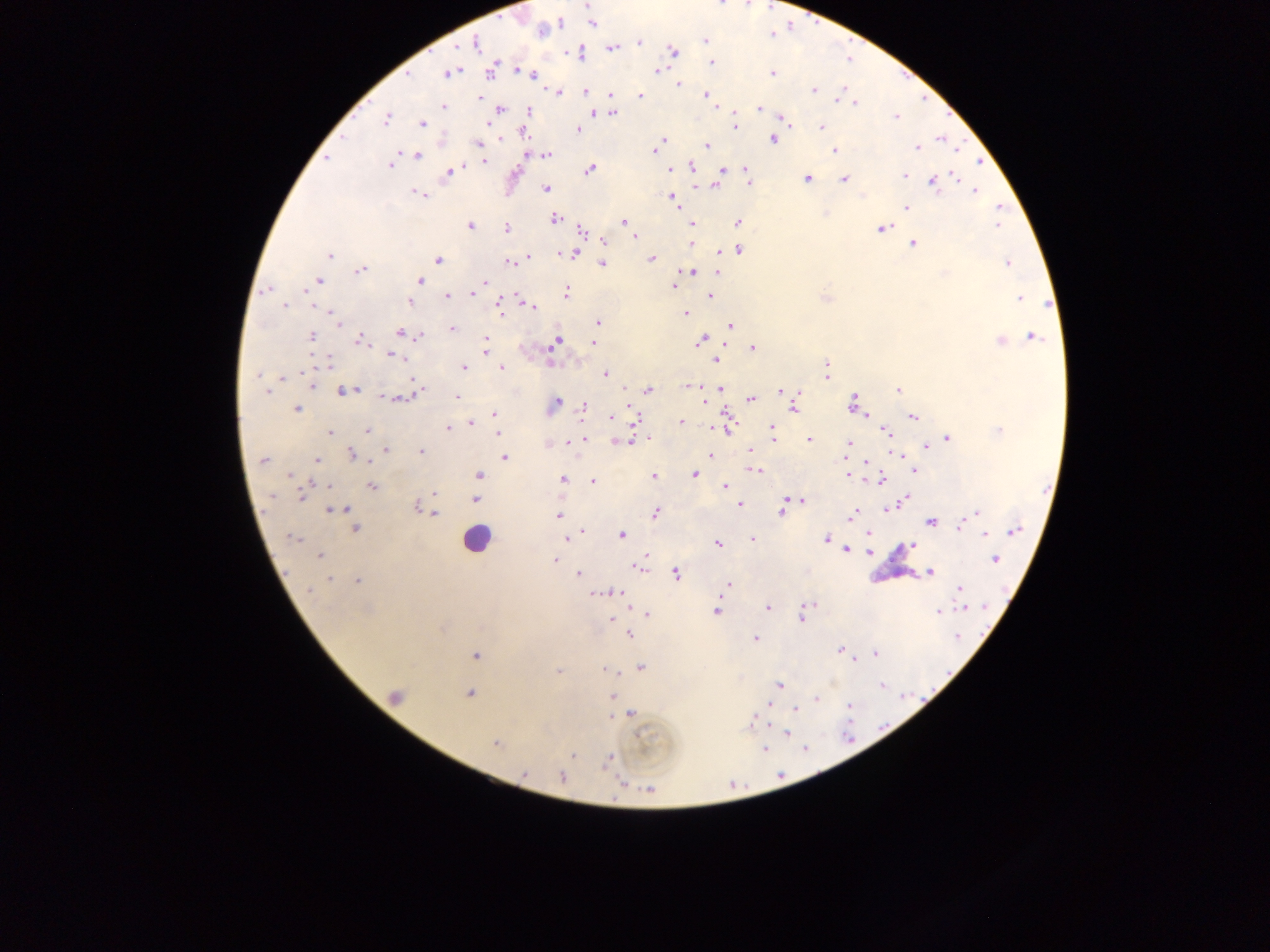
{
  "leukocyte_locations": "approximate centers as x y in pixels: 475 539",
  "plasmodium_parasite_locations": "approximate centers as x y in pixels: 587 5; 592 24; 542 30; 705 40; 639 42; 476 43; 612 49; 673 51; 579 53; 711 63; 491 70; 522 71; 658 71; 450 73; 772 73; 533 75; 679 85; 814 89; 558 92; 585 92; 611 95; 705 95; 641 96; 480 98; 855 103; 443 106; 759 109; 500 110; 530 110; 593 112; 613 113; 784 117; 896 117; 386 119; 490 123; 422 124; 734 126; 820 127; 579 129; 523 133; 664 140; 773 140; 942 140; 661 142; 479 144; 707 145; 917 148; 835 150; 655 151; 546 155; 417 156; 326 159; 484 161; 390 165; 691 167; 458 168; 589 170; 671 170; 450 171; 721 171; 746 171; 905 175; 955 176; 747 178; 807 178; 845 179; 934 183; 715 186; 545 189; 974 191; 418 194; 672 198; 907 207; 555 218; 624 222; 738 222; 692 224; 470 225; 998 226; 882 228; 507 229; 581 231; 633 235; 604 242; 692 243; 912 244; 739 250; 330 255; 573 255; 528 257; 651 259; 438 260; 509 262; 1007 263; 602 264; 360 271; 691 271; 717 273; 944 273; 318 280; 420 280; 485 282; 674 286; 266 290; 566 291; 473 293; 448 296; 710 296; 1020 298; 409 303; 284 306; 500 306; 531 307; 684 313; 333 316; 337 321; 599 322; 730 326; 452 329; 400 333; 311 336; 420 336; 1032 336; 360 340; 485 341; 700 341; 1000 341; 556 342; 593 344; 486 349; 753 349; 392 355; 715 361; 329 363; 827 366; 464 367; 501 367; 827 373; 605 374; 258 375; 282 377; 312 385; 690 385; 719 388; 898 389; 649 390; 266 391; 344 391; 781 391; 457 397; 397 398; 751 399; 558 401; 852 403; 585 406; 794 408; 297 409; 494 414; 611 417; 913 417; 635 419; 681 421; 471 422; 726 426; 448 428; 367 430; 772 430; 999 430; 886 431; 330 433; 497 433; 584 438; 948 438; 773 439; 578 440; 809 440; 621 441; 570 442; 850 443; 925 446; 386 450; 420 451; 750 451; 352 455; 709 455; 847 455; 897 455; 504 457; 317 460; 263 461; 867 462; 914 470; 756 471; 289 474; 694 474; 479 475; 848 475; 654 476; 563 479; 880 480; 593 481; 325 485; 372 486; 724 486; 434 493; 301 496; 475 499; 904 500; 803 501; 417 506; 740 506; 338 509; 887 509; 656 512; 781 512; 976 513; 433 514; 851 515; 558 516; 965 521; 931 522; 960 526; 355 528; 582 531; 1015 531; 986 533; 869 534; 574 535; 621 535; 294 539; 567 539; 753 539; 826 539; 718 544; 911 545; 847 550; 869 552; 319 556; 995 559; 555 560; 639 566; 930 572; 579 573; 676 574; 329 579; 358 581; 728 585; 959 588; 309 590; 604 592; 618 593; 768 607; 965 607; 804 610; 716 611; 938 612; 646 613; 801 616; 610 619; 630 634; 957 637; 756 638; 839 650; 875 654; 476 655; 641 668; 606 669; 558 671; 779 685; 882 686; 469 694; 394 696; 612 697; 816 698; 849 706; 796 709; 631 713; 613 715; 752 718; 786 732; 495 743; 764 749; 572 755; 608 759; 562 777; 649 790",
  "image_size": "1270×952 pixels",
  "preparation": "thick blood smear",
  "field_of_view": "single",
  "capture": "mobile-phone photograph through a microscope",
  "country": "Ghana"
}